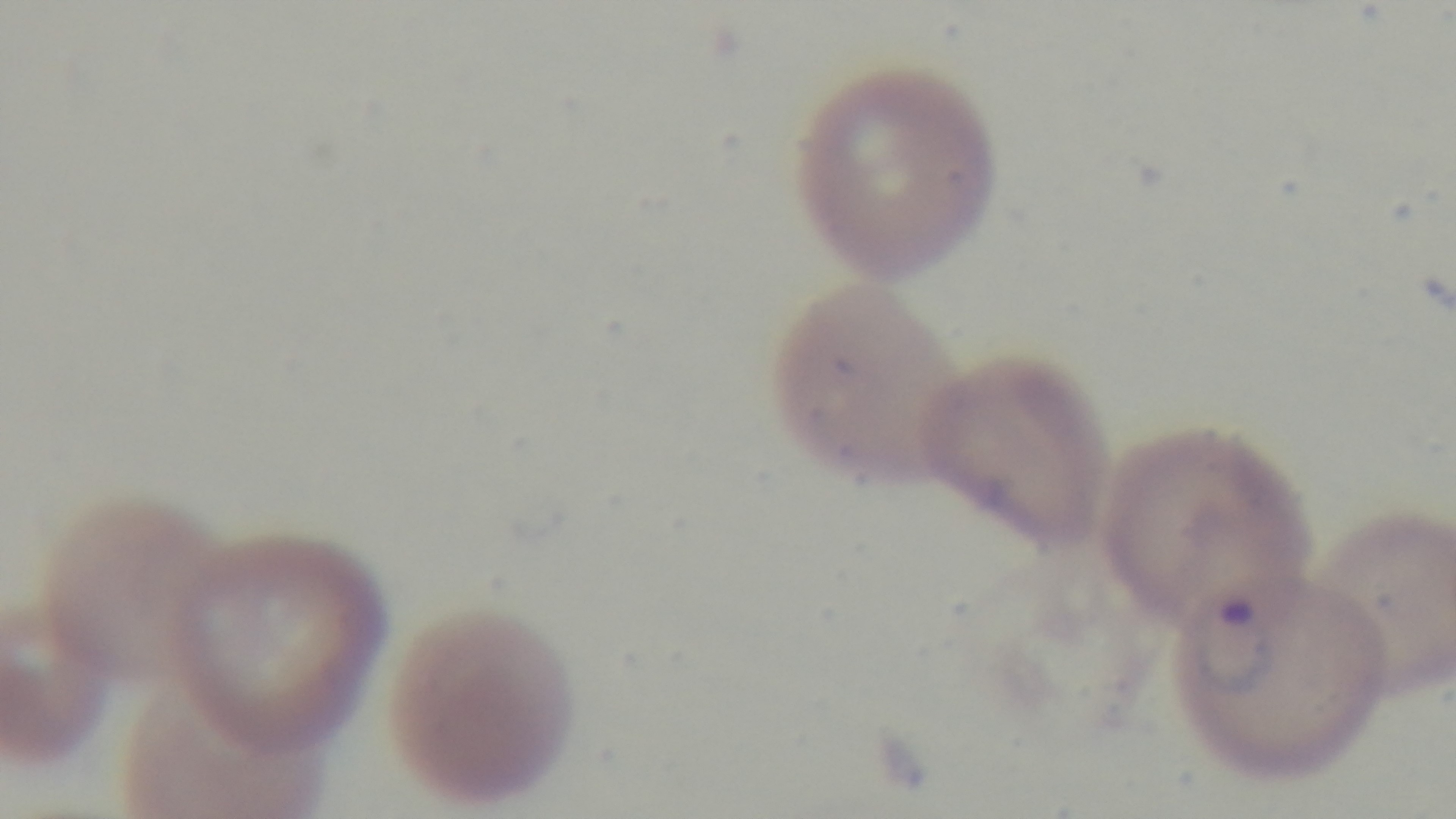
Summary:
  - Preparation: thin blood film
  - Malaria status: positive
  - Field of view: one from the slide
  - Modality: light microscopy
  - Stain: Giemsa
  - Objective: 100x oil immersion
  - Capture: mounted 4K digital camera